Comment on the morphology of the red blood cells.
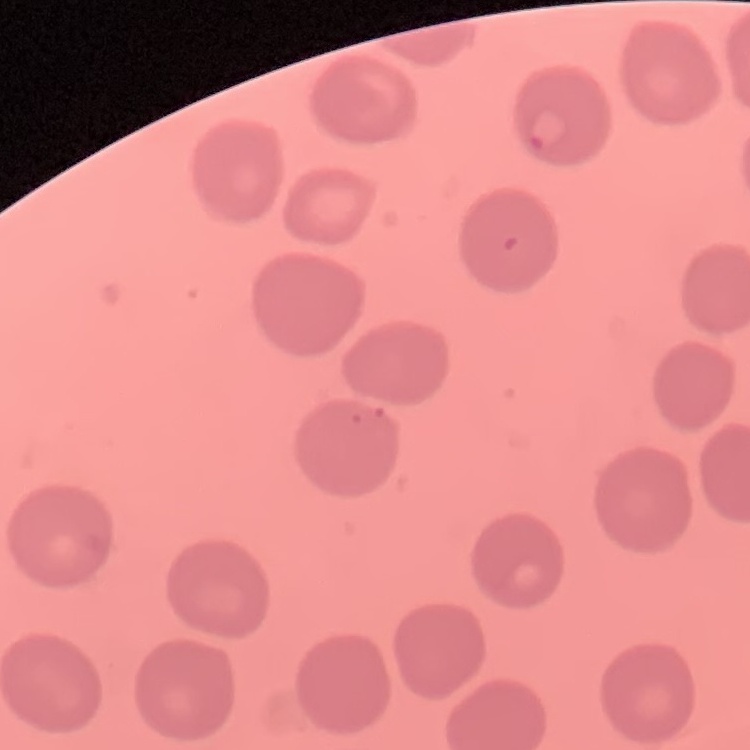

They show no rouleaux formation.

Summary:
  - Image type: one tile cut from a larger photomicrograph
  - Preparation: thin blood film
  - Stain: Field's or Giemsa